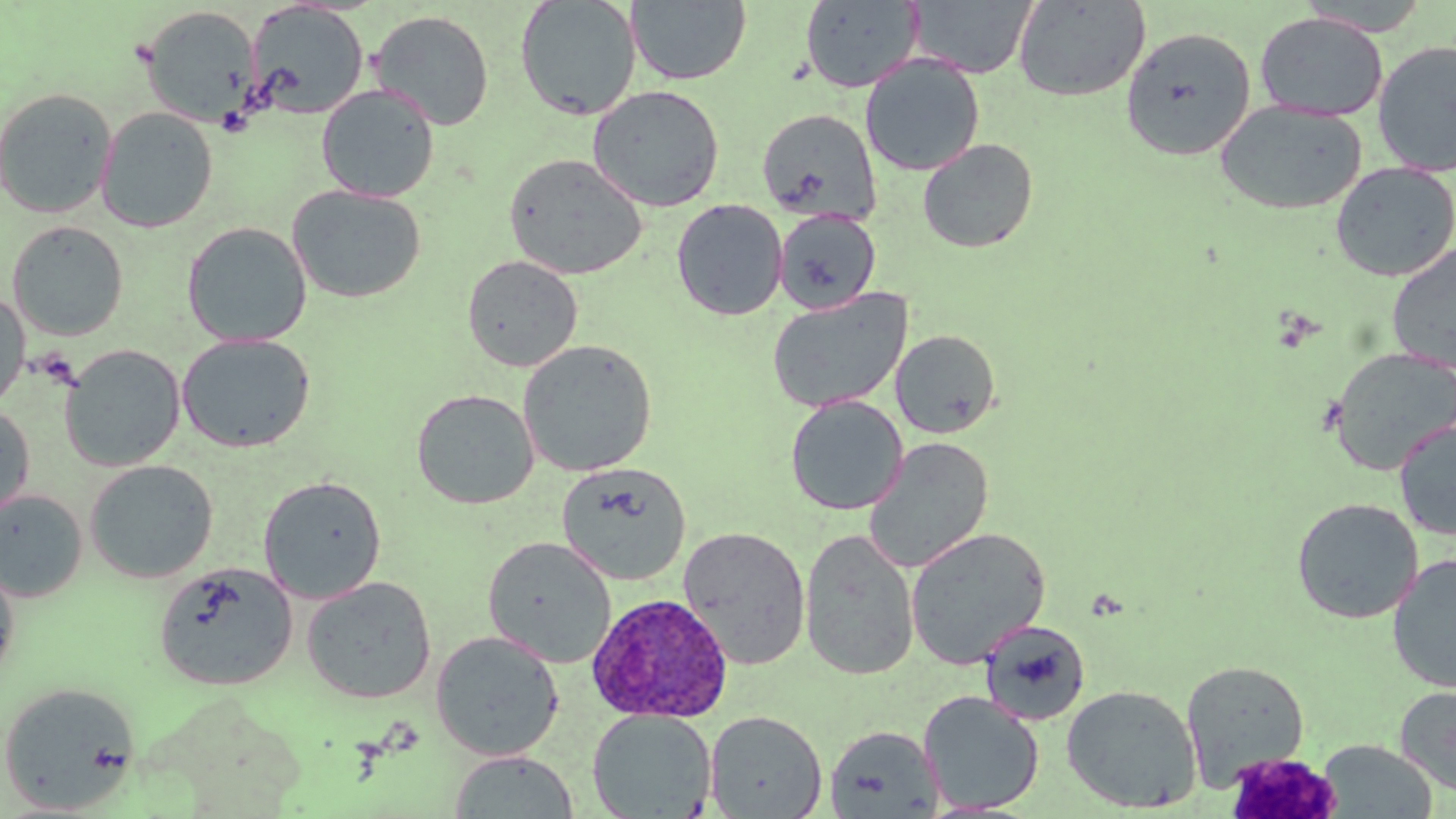

Summary:
  - Coordinate format: approximate bounding boxes as named x1/y1/x2/y2 corners in pixels
  - Uninfected red blood cell locations: (x1=626, y1=0, x2=751, y2=86), (x1=1013, y1=0, x2=1150, y2=102), (x1=1296, y1=0, x2=1433, y2=36), (x1=514, y1=1, x2=641, y2=121), (x1=799, y1=1, x2=923, y2=92), (x1=907, y1=1, x2=1037, y2=79), (x1=246, y1=2, x2=370, y2=119), (x1=140, y1=5, x2=259, y2=127), (x1=369, y1=9, x2=495, y2=131), (x1=1255, y1=12, x2=1389, y2=122), (x1=1121, y1=26, x2=1257, y2=161), (x1=1372, y1=39, x2=1456, y2=177), (x1=860, y1=54, x2=985, y2=176), (x1=317, y1=84, x2=440, y2=202), (x1=587, y1=84, x2=725, y2=212), (x1=0, y1=87, x2=117, y2=219), (x1=1215, y1=100, x2=1368, y2=215), (x1=97, y1=106, x2=218, y2=232), (x1=756, y1=107, x2=882, y2=225), (x1=917, y1=138, x2=1038, y2=253), (x1=503, y1=152, x2=648, y2=280), (x1=1330, y1=161, x2=1456, y2=282), (x1=287, y1=184, x2=426, y2=304), (x1=671, y1=198, x2=788, y2=320), (x1=774, y1=208, x2=881, y2=314), (x1=7, y1=220, x2=129, y2=341), (x1=182, y1=221, x2=312, y2=347), (x1=1386, y1=243, x2=1456, y2=374), (x1=462, y1=254, x2=583, y2=372), (x1=766, y1=289, x2=913, y2=414), (x1=0, y1=290, x2=30, y2=412), (x1=890, y1=329, x2=1002, y2=438), (x1=177, y1=333, x2=316, y2=453), (x1=517, y1=338, x2=658, y2=476), (x1=59, y1=344, x2=186, y2=472), (x1=1328, y1=347, x2=1456, y2=476), (x1=410, y1=388, x2=539, y2=509), (x1=785, y1=395, x2=908, y2=515), (x1=0, y1=405, x2=35, y2=524), (x1=1394, y1=419, x2=1456, y2=542), (x1=863, y1=436, x2=994, y2=574), (x1=84, y1=459, x2=219, y2=583), (x1=557, y1=461, x2=691, y2=585), (x1=257, y1=475, x2=387, y2=603), (x1=0, y1=490, x2=88, y2=602), (x1=1291, y1=497, x2=1423, y2=624), (x1=678, y1=525, x2=812, y2=670), (x1=906, y1=526, x2=1051, y2=670), (x1=799, y1=528, x2=920, y2=681), (x1=482, y1=536, x2=617, y2=668), (x1=1387, y1=553, x2=1456, y2=694), (x1=0, y1=559, x2=20, y2=687), (x1=154, y1=562, x2=298, y2=691), (x1=301, y1=575, x2=437, y2=704), (x1=980, y1=620, x2=1091, y2=726), (x1=430, y1=630, x2=564, y2=761), (x1=1181, y1=660, x2=1309, y2=789), (x1=0, y1=681, x2=142, y2=814), (x1=1061, y1=684, x2=1203, y2=813), (x1=1395, y1=685, x2=1456, y2=797), (x1=917, y1=690, x2=1044, y2=814), (x1=587, y1=708, x2=717, y2=819), (x1=705, y1=710, x2=827, y2=818), (x1=824, y1=724, x2=944, y2=818), (x1=1316, y1=739, x2=1438, y2=819), (x1=448, y1=750, x2=579, y2=818)
  - Platelet locations: (x1=1224, y1=751, x2=1343, y2=818)
  - Plasmodium ovale-infected red blood cell locations: (x1=587, y1=592, x2=733, y2=723)
  - Slide-level diagnosis: Plasmodium ovale
  - Image size: 1456×819 pixels
  - Magnification: 1000x
  - Modality: light microscopy
  - Stain: May-Grünwald-Giemsa
  - Field of view: single
  - Preparation: thin blood smear